Assess this cell for malaria.
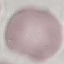
It is uninfected.

preparation = thin blood film
stain = Giemsa
image type = automatically extracted cell patch, resized to 64 × 64 pixels
capture = smartphone through the microscope eyepiece